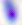 Toxoplasma gondii is shown. Micrograph. Captured at 400x magnification.